Assess this cell for malaria.
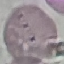

Uninfected.

Summary:
  - Capture: smartphone through the microscope eyepiece
  - Preparation: thin smear
  - Image type: automatically extracted cell patch, resized to 64 × 64 pixels
  - Stain: Giemsa